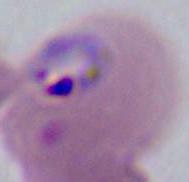
Summary:
  - Modality: photomicrograph
  - Identification: Plasmodium
  - Magnification: 400x or 1000x